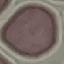
Summary:
  - Result: no malaria parasites detected
  - Image type: automatically extracted cell patch, resized to 64 × 64 pixels
  - Preparation: thin blood smear
  - Stain: Giemsa
  - Capture: smartphone camera at the microscope eyepiece